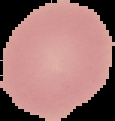
Summary:
  - Image size: 115×121 pixels
  - Image type: cell region segmented out of the field of view; surrounding area masked to black
  - Preparation: thin blood film
  - Result: no Plasmodium parasites detected